Classify this cell by malaria status.
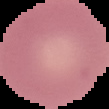

Uninfected.

Summary:
  - Image size: 109×109 pixels
  - Preparation: thin blood film
  - Image type: segmented cell region on a black background